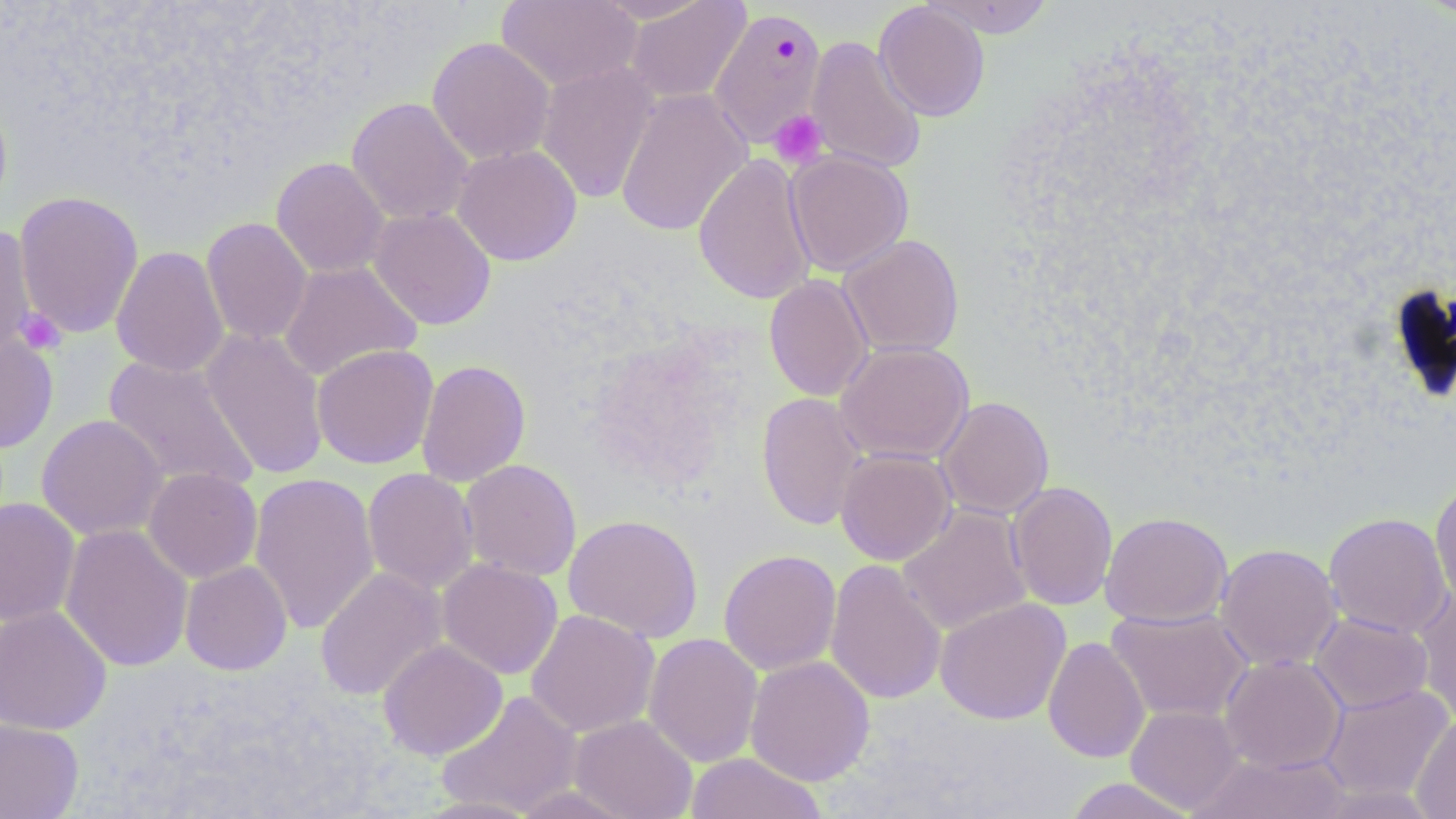

Summary:
  - Coordinate format: approximate bounding boxes as (x1,y1)-(x2,y2) corner pairs in pixels
  - Plasmodium falciparum-infected red blood cell locations: (709,7)-(827,149)
  - Uninfected red blood cell locations: (496,0)-(642,92), (592,0)-(715,23), (921,0)-(1055,38), (624,1)-(751,104), (874,1)-(991,122), (427,36)-(555,166), (806,37)-(927,174), (535,61)-(659,203), (615,87)-(753,237), (347,97)-(474,225), (451,144)-(582,266), (785,149)-(914,276), (693,153)-(817,305), (271,157)-(390,278), (13,190)-(144,339), (368,207)-(496,330), (201,216)-(313,346), (0,227)-(39,361), (838,234)-(965,358), (111,245)-(230,377), (278,260)-(422,381), (763,274)-(873,402), (201,328)-(330,480), (0,331)-(58,454), (835,341)-(974,464), (311,344)-(438,469), (102,354)-(261,494), (416,359)-(531,486), (756,391)-(869,531), (936,396)-(1055,519), (36,414)-(168,541), (834,448)-(957,565), (460,459)-(582,581), (143,467)-(262,583), (362,468)-(479,593), (249,471)-(380,634), (1430,480)-(1456,610), (1007,481)-(1118,611), (0,497)-(81,626), (898,505)-(1033,636), (1100,511)-(1232,627), (1323,512)-(1452,639), (563,514)-(703,642), (59,523)-(194,672), (1214,543)-(1342,671), (718,549)-(841,675), (437,558)-(563,679), (825,559)-(947,706), (180,560)-(292,675), (314,567)-(448,701), (1413,587)-(1456,725), (935,597)-(1071,725), (0,605)-(112,735), (1106,607)-(1252,724), (525,609)-(661,738), (1309,612)-(1433,714), (643,632)-(763,767), (1043,636)-(1150,763), (378,639)-(508,760), (745,655)-(875,786), (1219,655)-(1346,773), (1320,684)-(1453,801), (436,689)-(582,816), (1125,705)-(1245,814), (569,714)-(698,819), (1411,714)-(1456,818), (0,717)-(83,818), (685,752)-(828,818), (1189,752)-(1350,818), (1061,778)-(1201,818), (505,783)-(638,818), (414,796)-(543,818)
  - Platelet locations: (768,110)-(828,168), (16,309)-(66,354)
  - Slide-level diagnosis: Plasmodium falciparum
  - Field of view: one of a larger specimen
  - Preparation: thin blood smear
  - Stain: May-Grünwald-Giemsa
  - Modality: light microscopy
  - Image size: 1456×819 pixels
  - Magnification: 1000x